Classify this cell by malaria status.
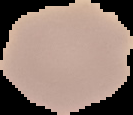

It is uninfected.

Summary:
  - Image type: segmented cell region with the area outside set to black
  - Image size: 133×115 pixels
  - Preparation: thin blood film